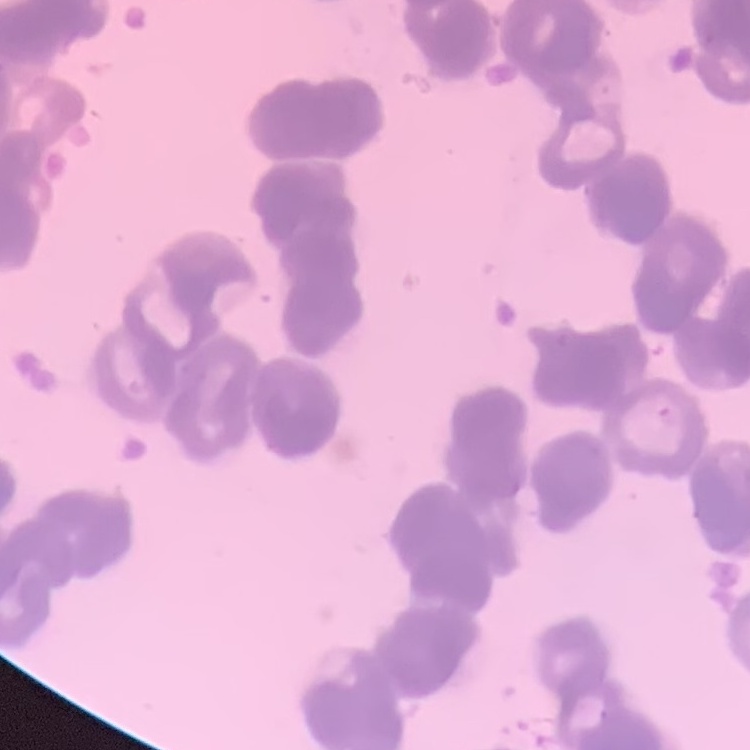
{
  "red_blood_cell_morphology": "rouleaux formation",
  "image_type": "one tile cut from a larger photomicrograph",
  "stain": "Field's or Giemsa",
  "preparation": "thin peripheral smear"
}